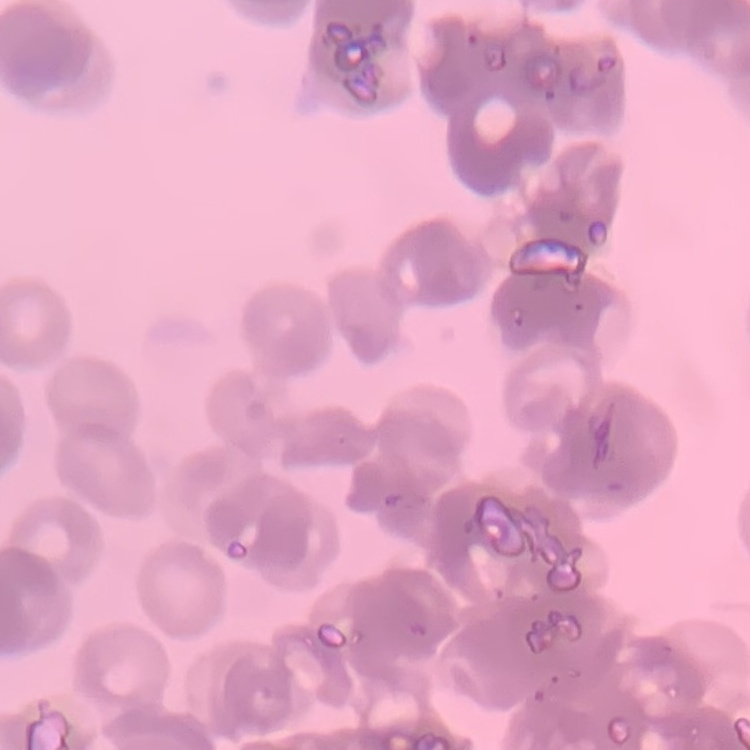
Summary:
  - Erythrocyte morphology: rouleaux formation
  - Preparation: thin blood film
  - Image type: one tile cut from a larger photomicrograph
  - Stain: Field's or Giemsa